Locate every uninfected red blood cell.
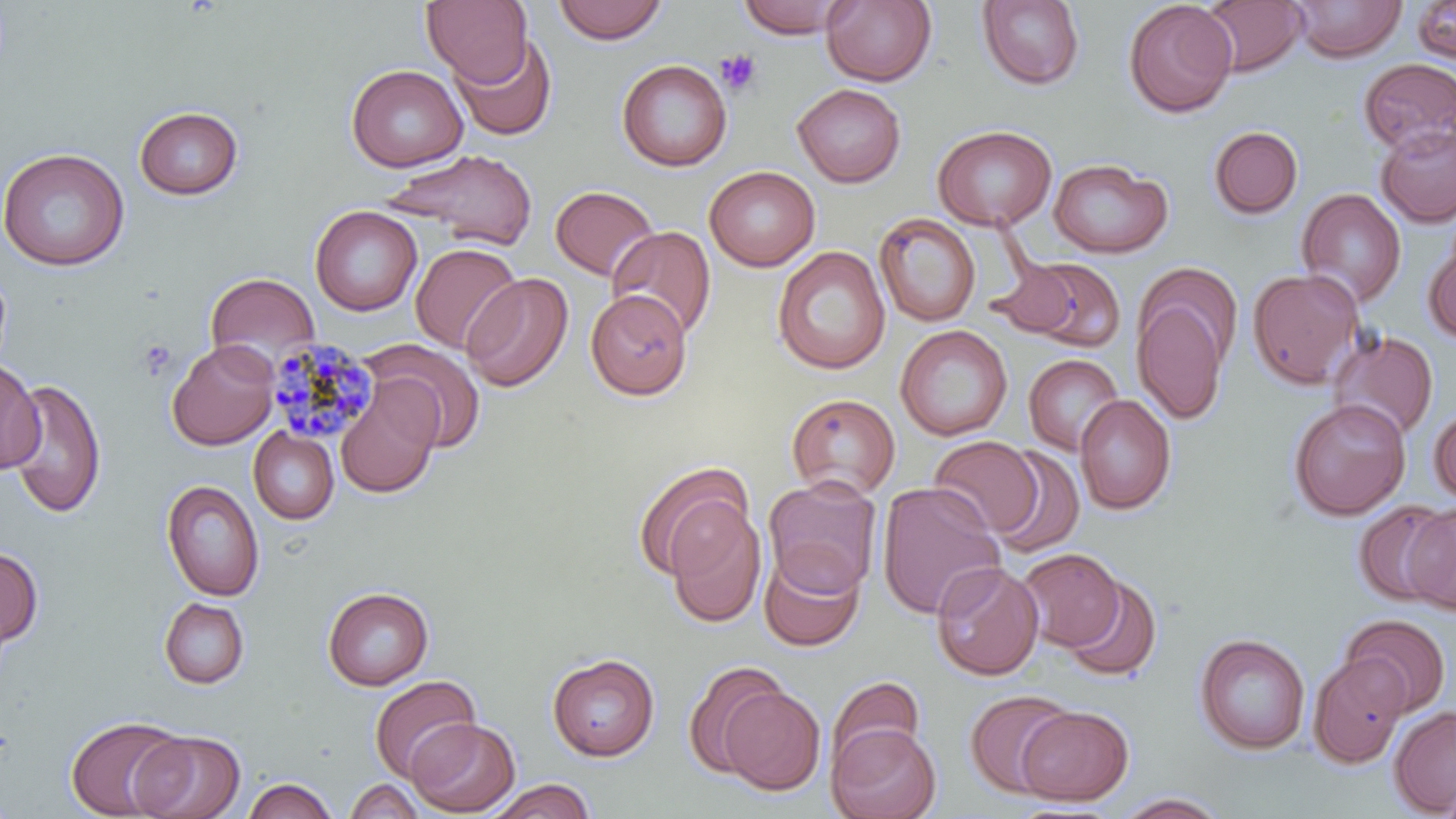

Approximate bounding boxes as [x1, y1, x2, y2] in pixels.
Uninfected red blood cells: [421, 0, 532, 85], [735, 0, 856, 39], [820, 0, 937, 87], [1123, 0, 1238, 118], [1289, 0, 1407, 63], [552, 1, 669, 45], [976, 1, 1086, 90], [1200, 1, 1307, 76], [1412, 1, 1455, 65], [449, 33, 557, 142], [616, 58, 732, 172], [1358, 58, 1456, 157], [346, 64, 468, 172], [792, 83, 906, 187], [133, 105, 244, 200], [932, 124, 1057, 231], [1208, 125, 1303, 220], [1375, 125, 1456, 227], [0, 147, 129, 271], [386, 148, 538, 250], [1048, 158, 1172, 258], [704, 166, 820, 271], [550, 185, 659, 281], [1296, 187, 1406, 308], [310, 206, 422, 316], [874, 213, 980, 327], [606, 226, 717, 339], [1423, 237, 1456, 343], [410, 243, 522, 354], [772, 246, 890, 375], [1009, 259, 1126, 352], [1247, 268, 1364, 391], [205, 271, 320, 371], [461, 273, 573, 393], [1133, 281, 1233, 426], [586, 290, 692, 399], [895, 325, 1012, 441], [1327, 330, 1439, 441], [167, 339, 279, 450], [363, 339, 487, 453], [1023, 354, 1125, 456], [0, 358, 43, 475], [6, 379, 107, 519], [335, 382, 441, 499], [785, 393, 901, 500], [1075, 394, 1176, 515], [1288, 398, 1411, 521], [1429, 405, 1456, 505], [248, 426, 339, 524], [928, 436, 1043, 538], [987, 446, 1085, 558], [633, 462, 753, 580], [763, 476, 882, 597], [161, 479, 265, 601], [876, 481, 1005, 620], [1352, 501, 1453, 606], [665, 503, 767, 628], [1403, 505, 1456, 615], [0, 545, 43, 649], [1018, 548, 1125, 652], [759, 549, 865, 652], [932, 562, 1043, 681], [1061, 574, 1162, 683], [322, 586, 434, 690], [158, 598, 249, 689], [1340, 614, 1451, 717], [1194, 633, 1310, 755], [547, 653, 659, 761], [1308, 654, 1410, 769], [683, 660, 791, 779], [369, 674, 481, 783], [827, 676, 926, 772], [719, 686, 826, 795], [965, 689, 1076, 799], [1015, 706, 1135, 805], [1388, 706, 1456, 816], [64, 715, 187, 819], [406, 717, 520, 816], [827, 724, 941, 819], [131, 729, 246, 819], [242, 777, 337, 819], [344, 779, 425, 818], [484, 779, 597, 818], [1438, 780, 1456, 819], [1113, 792, 1230, 818].

{
  "plasmodium_malariae_infected_red_blood_cell_locations": "approximate bounding boxes as [x1, y1, x2, y2] in pixels: [266, 338, 378, 447]",
  "slide_level_diagnosis": "Plasmodium malariae",
  "preparation": "thin blood film",
  "magnification": "1000x",
  "image_size": "1456×819 pixels",
  "platelet_locations": "approximate bounding boxes as [x1, y1, x2, y2] in pixels: [715, 49, 762, 96], [137, 339, 176, 381]",
  "field_of_view": "one of a larger specimen",
  "modality": "optical microscopy",
  "stain": "May-Grünwald-Giemsa"
}